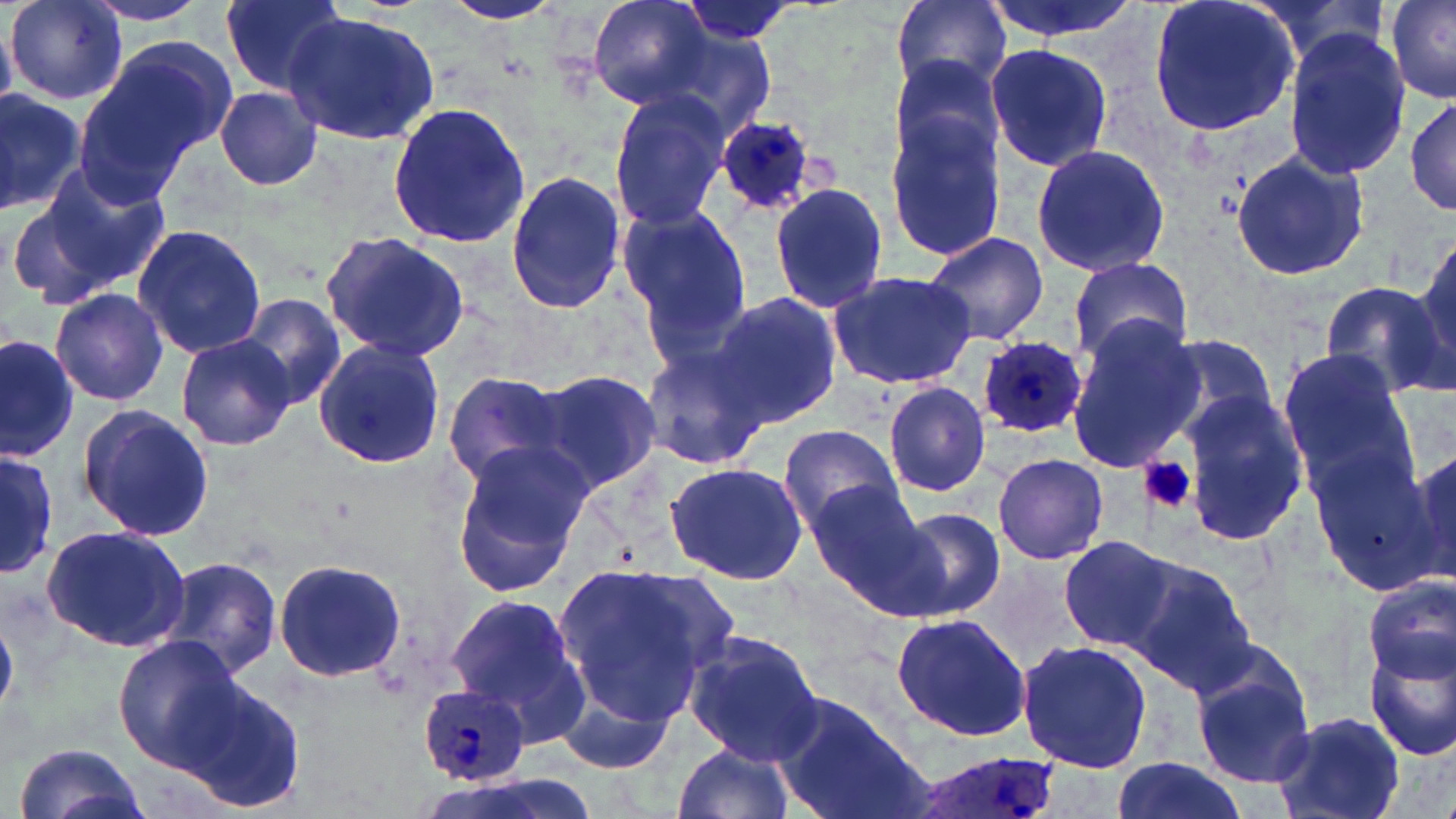
Approximate bounding boxes as [x1, y1, x2, y2] in pixels. Platelet locations: [1139, 458, 1197, 515]. Plasmodium ovale-infected red blood cell locations: [713, 114, 821, 215], [976, 336, 1085, 437], [419, 685, 533, 785], [902, 752, 1065, 819]. Uninfected red blood cell locations: [7, 0, 126, 104], [220, 0, 346, 93], [585, 0, 713, 111], [889, 0, 1012, 94], [980, 0, 1141, 43], [1146, 0, 1302, 140], [1387, 0, 1456, 102], [82, 1, 211, 27], [442, 1, 563, 27], [678, 2, 799, 47], [281, 11, 440, 144], [647, 23, 777, 143], [1282, 28, 1414, 184], [73, 40, 225, 202], [985, 43, 1111, 174], [887, 54, 1009, 171], [214, 85, 323, 193], [0, 86, 83, 212], [606, 89, 734, 231], [1407, 95, 1455, 218], [386, 101, 531, 250], [884, 109, 1008, 263], [1031, 144, 1172, 278], [1230, 149, 1367, 282], [30, 158, 173, 297], [504, 169, 627, 314], [769, 184, 887, 315], [1, 188, 130, 313], [616, 205, 752, 344], [132, 225, 266, 359], [922, 230, 1049, 347], [1411, 231, 1455, 383], [318, 233, 470, 362], [1066, 256, 1197, 368], [825, 269, 979, 391], [1316, 282, 1449, 395], [49, 285, 169, 406], [709, 292, 843, 430], [240, 294, 347, 410], [1064, 321, 1205, 471], [0, 332, 79, 464], [1155, 332, 1281, 443], [175, 335, 297, 451], [312, 339, 446, 469], [643, 344, 769, 471], [1277, 348, 1415, 496], [535, 369, 662, 495], [441, 370, 573, 485], [882, 381, 991, 497], [1179, 392, 1311, 546], [77, 406, 216, 542], [775, 423, 903, 533], [1308, 438, 1444, 596], [450, 441, 592, 595], [1406, 442, 1453, 580], [0, 452, 59, 577], [992, 453, 1107, 565], [663, 460, 810, 585], [806, 481, 932, 605], [888, 507, 1006, 621], [40, 524, 193, 651], [1057, 535, 1184, 651], [159, 554, 283, 680], [271, 556, 406, 684], [1121, 559, 1258, 697], [552, 563, 726, 726], [1361, 573, 1454, 686], [443, 591, 586, 731], [889, 611, 1033, 744], [682, 630, 824, 762], [113, 636, 241, 768], [1016, 640, 1156, 775], [1364, 644, 1456, 762], [1190, 649, 1316, 790], [179, 677, 305, 816], [556, 682, 677, 776], [768, 692, 924, 819], [1272, 711, 1407, 819], [14, 741, 146, 819], [671, 743, 796, 819], [1112, 756, 1244, 818], [418, 773, 606, 819]. Slide-level diagnosis: Plasmodium ovale. Single field of view. 1000x magnification. Thin blood smear. May-Grünwald-Giemsa stain. Optical microscopy. Image is 1456×819 pixels.